Comment on the morphology of the red blood cells.
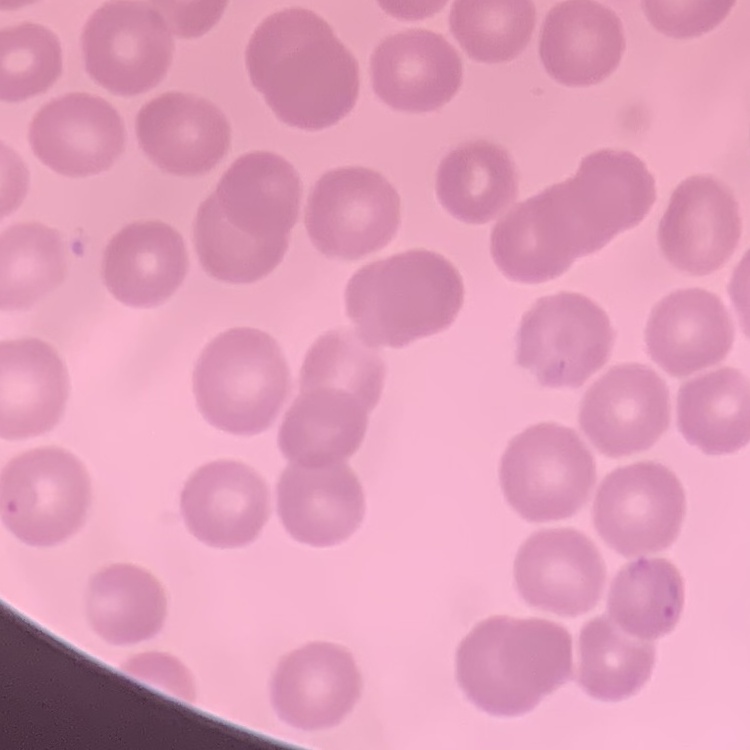

No rouleaux formation.

image type = square crop of a larger photomicrograph
preparation = thin blood film
stain = Field's or Giemsa